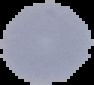
From a thin blood film. The area outside the segmented cell region is set to black. Malaria status: uninfected. Image is 94×85 pixels.